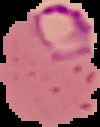 Result: malaria parasites detected. From a thin blood film. Image is 100×127 pixels. Cell region segmented out of the field of view; the surrounding area is masked to black.